Point out each Plasmodium parasite.
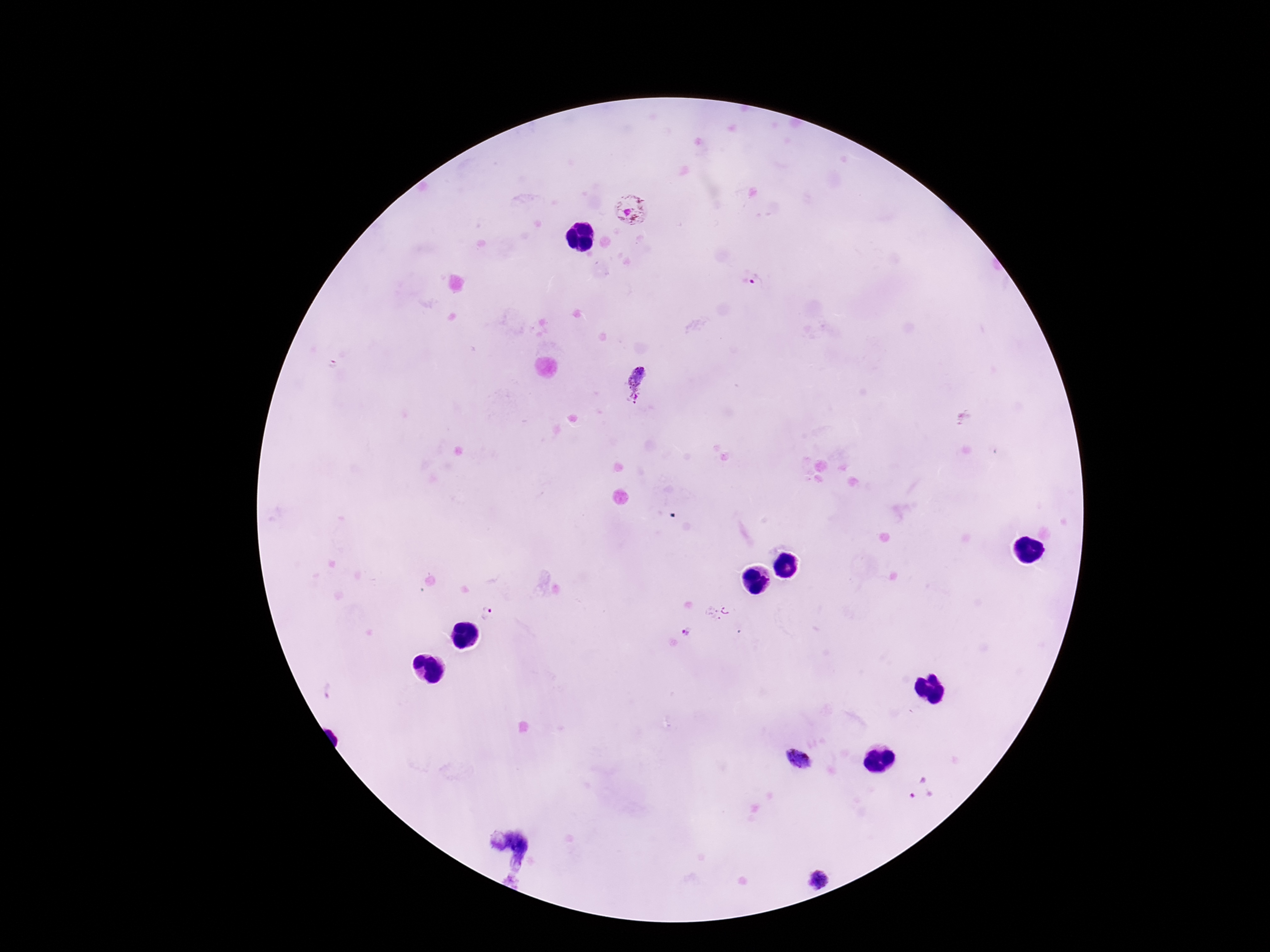

Approximate centers as {x, y} in pixels.
Plasmodium parasites: {630, 211}, {759, 283}, {640, 384}, {720, 613}, {488, 616}, {688, 633}, {799, 761}, {920, 790}, {508, 847}, {816, 880}.

stain = Giemsa
capture = smartphone camera through the microscope eyepiece
magnification = 100x
preparation = thick blood film
image size = 1270×952 pixels
field of view = single
patient malaria status = infected